Comment on the morphology of the red blood cells.
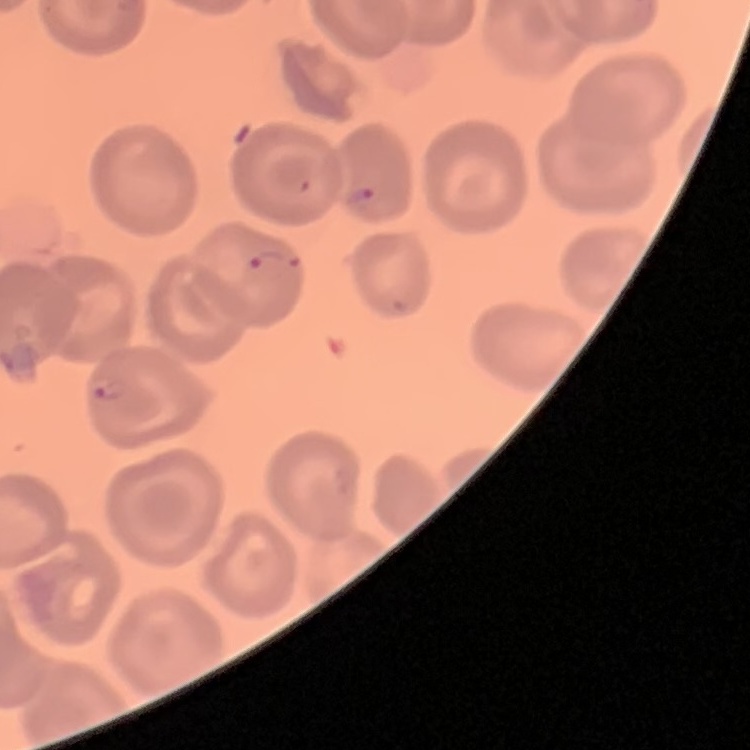

They show no rouleaux formation.

stain = Field's or Giemsa
preparation = thin blood film
image type = square crop of a larger photomicrograph